Mark where platelets are.
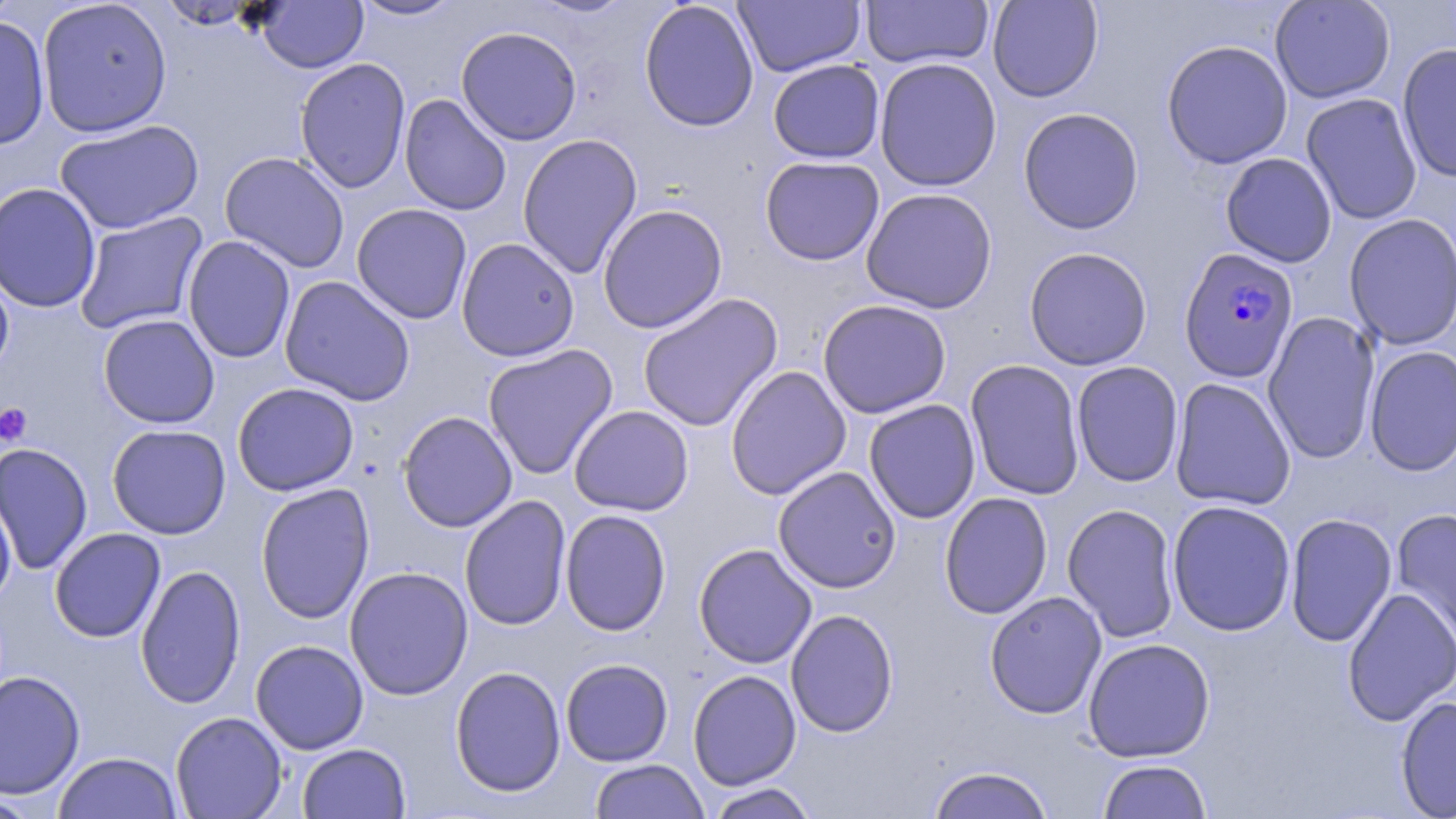

Approximate bounding boxes as (x1,y1)-(x2,y2) corner pairs in pixels.
Platelets: (0,402)-(33,446).

slide-level diagnosis = Plasmodium falciparum
uninfected red blood cell locations = approximate bounding boxes as (x1,y1)-(x2,y2) corner pairs in pixels: (0,0)-(21,28), (37,0)-(173,137), (350,0)-(463,21), (527,0)-(636,18), (639,0)-(759,132), (861,0)-(993,69), (987,0)-(1104,102), (1269,0)-(1396,104), (156,1)-(264,29), (255,1)-(368,73), (733,1)-(865,77), (0,14)-(51,152), (456,26)-(582,146), (1161,40)-(1293,169), (1397,43)-(1456,183), (295,57)-(411,194), (874,57)-(1002,191), (768,59)-(885,163), (399,93)-(512,215), (1300,93)-(1422,224), (1018,107)-(1144,234), (54,119)-(204,235), (517,133)-(642,279), (219,151)-(350,273), (1220,152)-(1337,267), (760,156)-(884,266), (0,182)-(102,313), (861,188)-(997,313), (351,203)-(472,324), (597,204)-(728,333), (74,211)-(210,335), (1343,213)-(1456,350), (182,235)-(296,364), (456,237)-(580,362), (1024,247)-(1152,370), (0,266)-(15,380), (279,275)-(415,406), (637,293)-(783,433), (817,299)-(952,419), (1262,311)-(1380,464), (98,314)-(220,429), (482,344)-(618,480), (1364,345)-(1456,477), (965,358)-(1085,501), (1071,361)-(1184,487), (725,365)-(852,500), (1170,378)-(1296,511), (232,382)-(359,496), (864,399)-(981,524), (569,405)-(694,516), (397,410)-(518,532), (106,424)-(232,539), (0,442)-(93,576), (773,466)-(901,593), (255,483)-(375,624), (0,490)-(16,607), (938,492)-(1053,620), (460,494)-(572,631), (1168,500)-(1296,636), (1062,503)-(1180,643), (1392,507)-(1456,650), (559,509)-(672,636), (1284,512)-(1397,648), (49,527)-(166,643), (693,543)-(817,669), (135,563)-(246,709), (344,566)-(473,700), (1341,587)-(1456,727), (984,591)-(1107,719), (785,609)-(899,738), (1083,637)-(1215,762), (250,640)-(369,754), (560,658)-(673,766), (450,666)-(566,797), (687,669)-(802,790), (0,670)-(86,800), (1395,695)-(1456,819), (170,711)-(288,818), (298,743)-(410,818), (53,751)-(183,818), (589,759)-(709,819), (1098,759)-(1212,818), (926,765)-(1056,819), (706,782)-(821,818), (0,792)-(48,818)
stain = May-Grünwald-Giemsa
modality = optical microscopy
magnification = 1000x
field of view = one of a larger specimen
image size = 1456×819 pixels
preparation = thin blood film
Plasmodium falciparum-infected red blood cell locations = approximate bounding boxes as (x1,y1)-(x2,y2) corner pairs in pixels: (1179,247)-(1299,384)